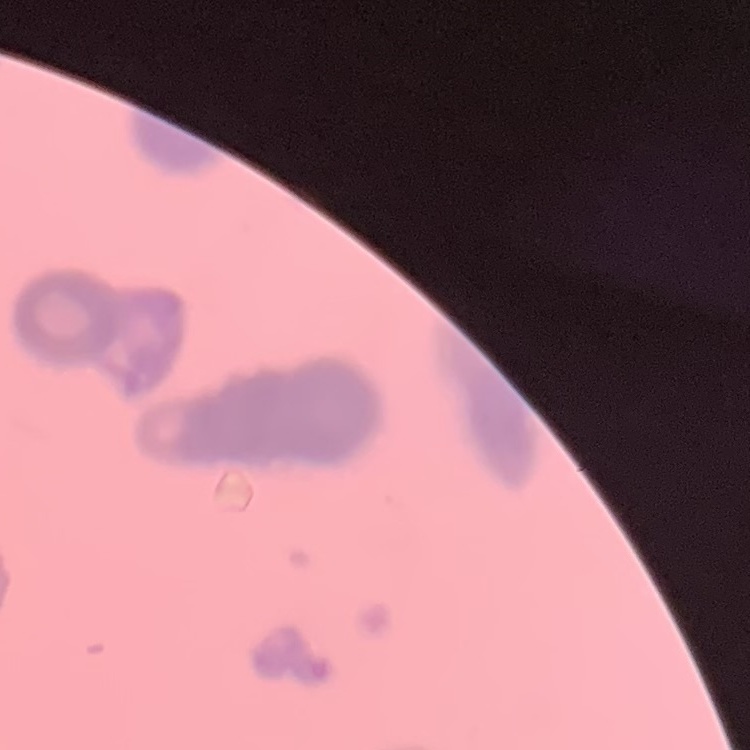 The red blood cells show rouleaux formation. Field's or Giemsa stain. Square crop of a larger photomicrograph. Thin peripheral smear.